Assess the morphology of the erythrocytes.
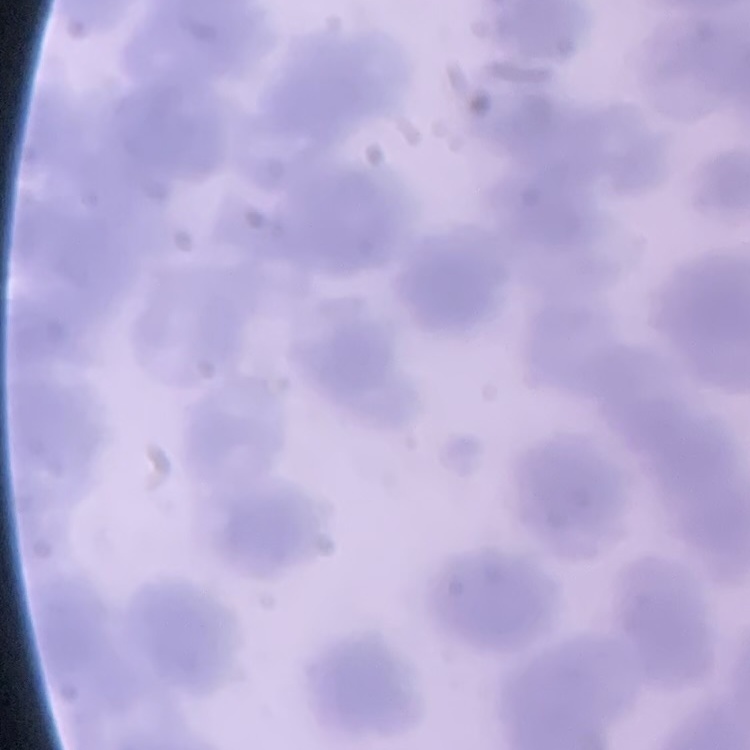

Rouleaux formation.

Thin blood smear. Square crop of a larger photomicrograph. Field's or Giemsa stain.